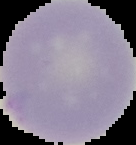

Summary:
  - Image size: 136×145 pixels
  - Image type: cell region segmented out of the field of view; surrounding area masked to black
  - Malaria status: uninfected
  - Preparation: thin blood smear